Assess for Plasmodium parasites.
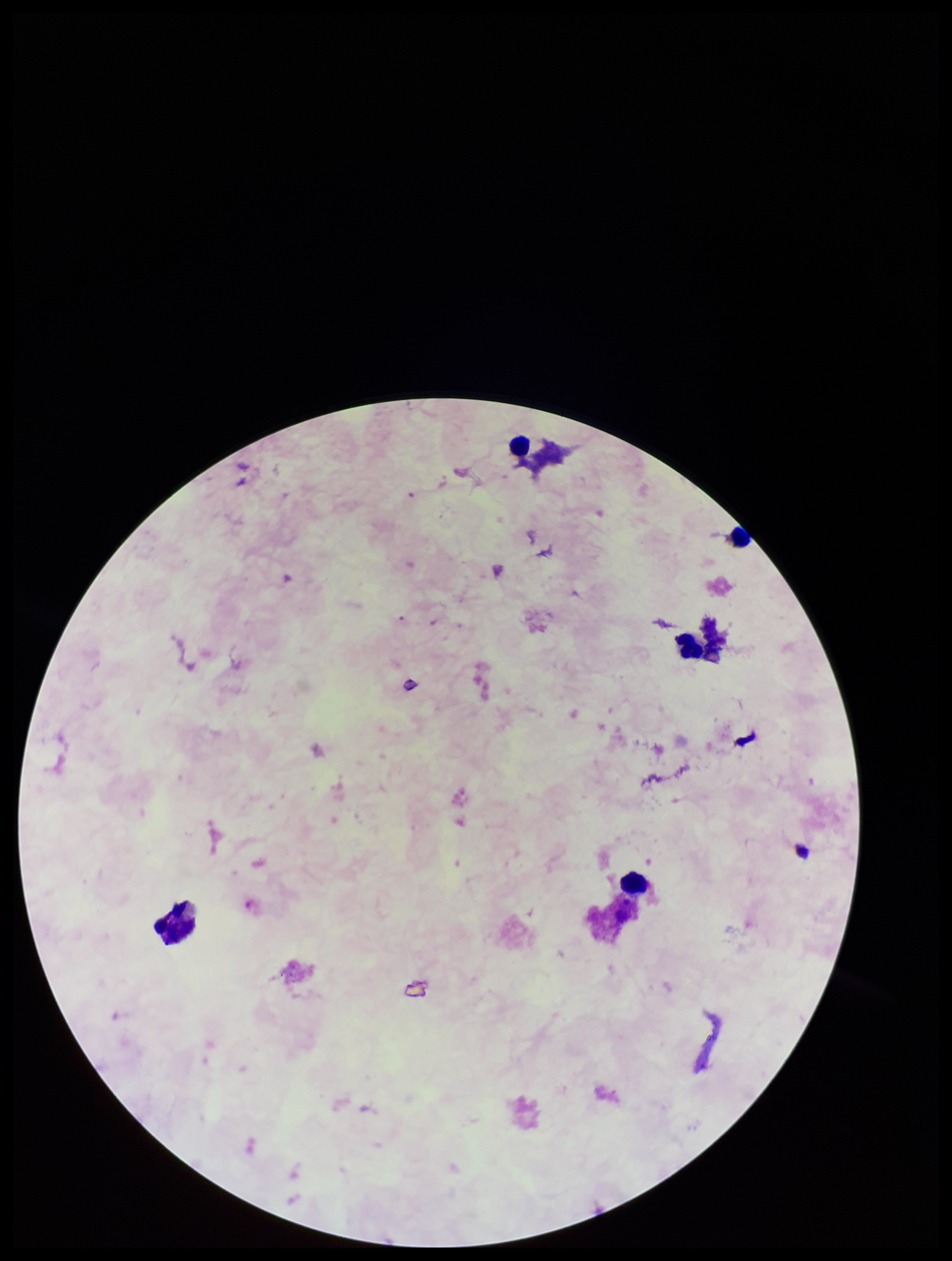

None detected.

field of view = one from this slide
parasite count = 0
capture = smartphone photograph through the microscope eyepiece
leukocyte count = 4
image size = 952×1261 pixels
preparation = thick smear
stain = Giemsa
patient malaria status = negative